Identify the cell.
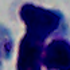
A leukocyte.

modality: micrograph
magnification: 1000x